Outline each blood parasite and name the species.
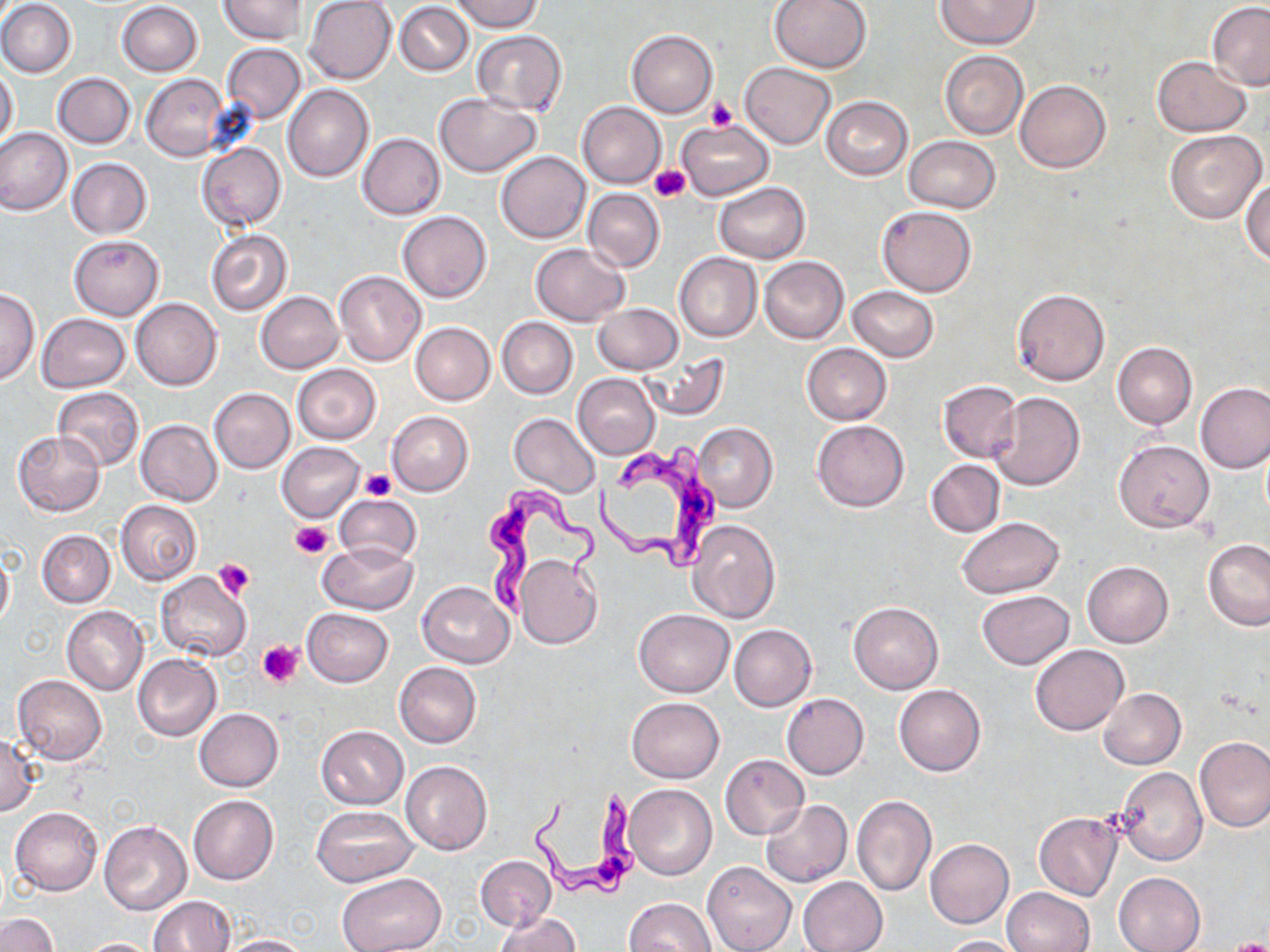
Approximate bounding boxes as [x1, y1, x2, y2] in pixels.
Trypanosoma brucei: [598, 446, 717, 576], [479, 486, 599, 618], [526, 785, 645, 899].
No Plasmodium falciparum, Plasmodium ovale, Plasmodium malariae, Plasmodium vivax, or Babesia divergens observed.

Platelet locations: [706, 97, 736, 130], [650, 165, 690, 203], [361, 470, 396, 500], [292, 521, 333, 559], [213, 558, 255, 599], [258, 640, 303, 685], [1226, 938, 1270, 952]. Uninfected red blood cell locations: [220, 0, 308, 44], [449, 0, 543, 32], [769, 0, 871, 73], [936, 0, 1041, 49], [1, 1, 76, 78], [306, 1, 397, 84], [116, 2, 203, 77], [396, 2, 472, 76], [1207, 2, 1270, 89], [470, 30, 567, 116], [627, 30, 717, 117], [222, 42, 305, 124], [940, 52, 1028, 139], [1152, 57, 1251, 136], [739, 62, 836, 149], [0, 66, 19, 149], [53, 72, 135, 149], [141, 74, 230, 161], [1014, 81, 1110, 172], [282, 84, 373, 182], [433, 92, 541, 176], [822, 96, 912, 180], [578, 101, 666, 189], [676, 120, 773, 200], [0, 126, 73, 215], [1165, 130, 1267, 223], [357, 132, 446, 219], [904, 135, 1000, 214], [197, 142, 286, 230], [496, 151, 590, 243], [67, 158, 152, 238], [1242, 177, 1270, 265], [714, 182, 809, 262], [583, 189, 664, 271], [877, 206, 976, 296], [398, 210, 491, 303], [206, 231, 292, 316], [69, 235, 163, 319], [530, 242, 629, 326], [674, 252, 762, 342], [758, 256, 849, 343], [334, 269, 427, 367], [848, 286, 939, 362], [0, 288, 41, 384], [1011, 289, 1109, 386], [256, 291, 343, 373], [131, 297, 223, 390], [592, 303, 683, 375], [36, 313, 129, 392], [496, 317, 577, 399], [409, 322, 495, 405], [1113, 342, 1196, 429], [801, 343, 890, 425], [638, 349, 729, 419], [293, 364, 381, 444], [572, 373, 661, 459], [938, 380, 1022, 462], [1196, 383, 1270, 473], [52, 386, 144, 471], [210, 388, 294, 473], [989, 392, 1084, 491], [386, 411, 473, 496], [510, 414, 600, 499], [136, 419, 222, 507], [812, 419, 909, 511], [695, 423, 777, 511], [13, 430, 105, 515], [1115, 439, 1214, 533], [277, 440, 366, 522], [925, 459, 1005, 537], [334, 494, 421, 567], [116, 500, 201, 586], [957, 518, 1064, 598], [687, 519, 781, 623], [37, 529, 114, 607], [1203, 538, 1270, 629], [317, 542, 419, 615], [0, 547, 13, 631], [516, 553, 602, 649], [1082, 561, 1173, 646], [155, 570, 251, 661], [417, 581, 514, 668], [977, 590, 1073, 669], [848, 601, 943, 694], [61, 606, 148, 695], [302, 608, 393, 687], [634, 608, 733, 697], [729, 624, 816, 712], [1030, 644, 1127, 735], [133, 654, 221, 740], [394, 662, 482, 747], [13, 675, 107, 764], [894, 684, 986, 775], [1099, 687, 1186, 769], [782, 693, 869, 779], [627, 697, 724, 782], [194, 708, 283, 791], [315, 724, 408, 809], [0, 733, 39, 816], [1194, 736, 1270, 832], [721, 754, 808, 839], [400, 760, 492, 855], [1115, 767, 1207, 865], [625, 783, 716, 880], [188, 795, 278, 885], [851, 796, 936, 896], [759, 800, 851, 888], [312, 805, 417, 886], [11, 806, 103, 896], [1035, 813, 1123, 900], [99, 821, 192, 915], [925, 838, 1015, 929], [475, 854, 554, 931], [703, 861, 795, 952], [1113, 872, 1206, 952], [336, 873, 444, 952], [798, 876, 888, 952], [622, 886, 787, 952], [1002, 888, 1094, 951], [149, 895, 234, 951], [625, 897, 716, 950], [496, 911, 580, 952], [0, 913, 57, 951], [220, 933, 309, 951], [939, 935, 1027, 951], [72, 938, 163, 952]. Slide-level diagnosis: Trypanosoma brucei. Image is 1270×952 pixels. Optical microscopy. May-Grünwald-Giemsa stain. Single field of view. Thin blood smear. 1000x magnification.